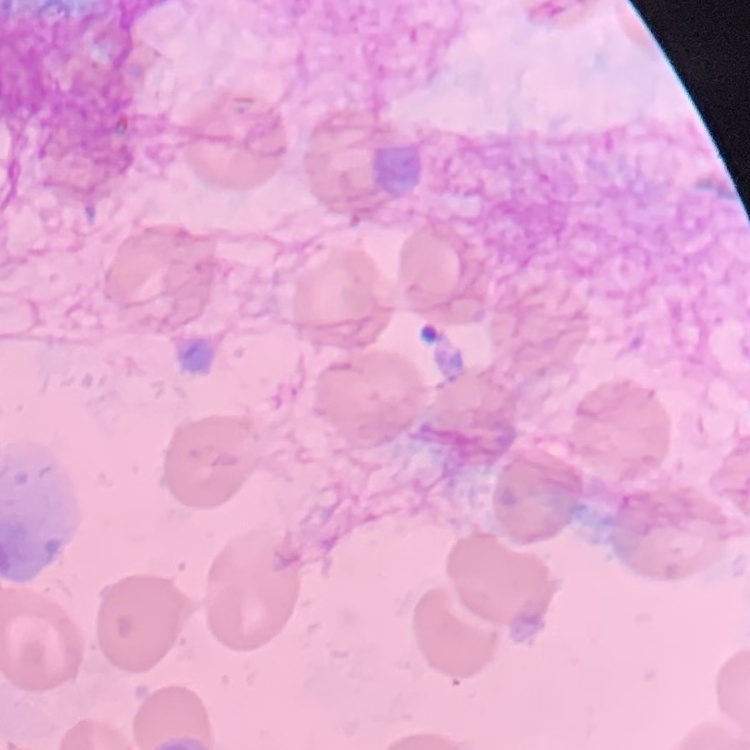

{
  "erythrocyte_morphology": "no rouleaux formation",
  "stain": "Field's or Giemsa",
  "preparation": "thin blood smear",
  "image_type": "square crop of a larger photomicrograph"
}